Comment on the morphology of the red blood cells.
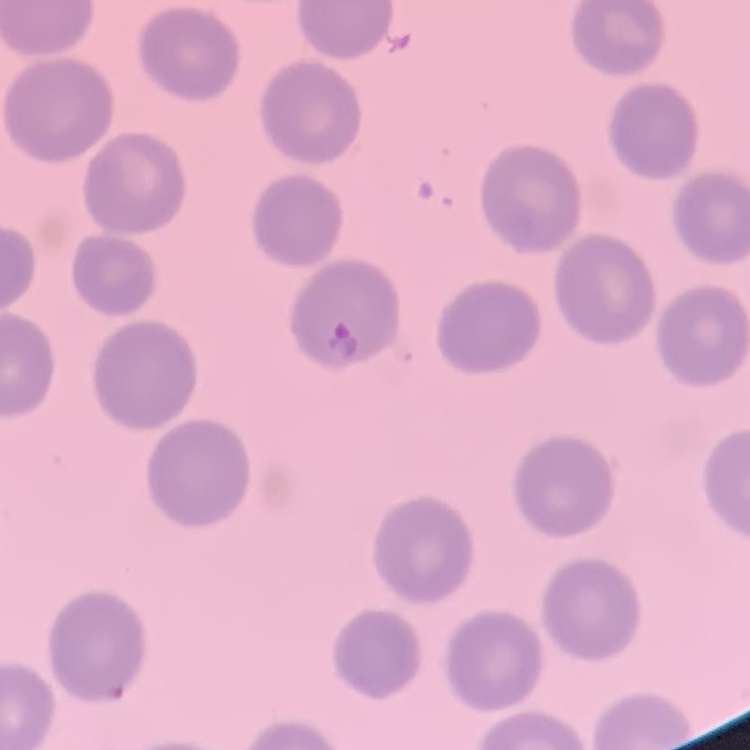
They show no rouleaux formation.

image type = square crop of a larger photomicrograph
stain = Field's or Giemsa
preparation = thin blood film